Report the malaria status of this cell.
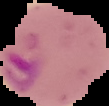

Parasitized.

image size = 109×106 pixels
preparation = thin blood smear
image type = segmented cell region with the area outside set to black